Name the parasite shown.
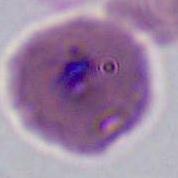
Plasmodium.

Summary:
  - Magnification: 400x or 1000x
  - Modality: micrograph